Locate and identify every blood parasite.
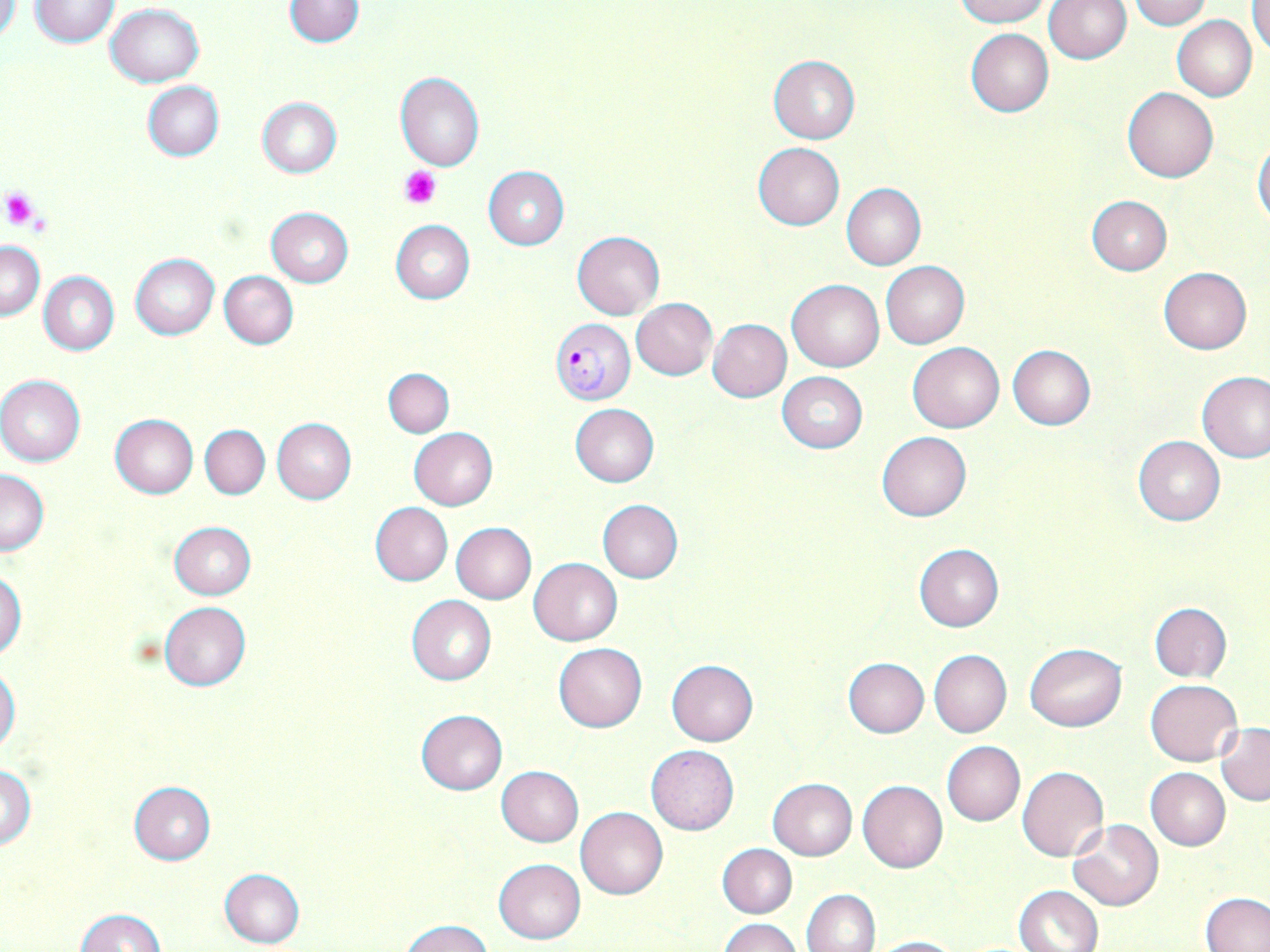
Approximate bounding boxes as (x1,y1)-(x2,y2) corner pairs in pixels.
Plasmodium falciparum-infected red blood cells: (549,318)-(634,404).
No Plasmodium ovale, Plasmodium malariae, Plasmodium vivax, Babesia divergens, or Trypanosoma brucei observed.

slide-level diagnosis = Plasmodium falciparum
preparation = thin blood smear
image size = 1270×952 pixels
stain = May-Grünwald-Giemsa
field of view = single
modality = optical microscopy
magnification = 1000x
uninfected red blood cell locations = approximate bounding boxes as (x1,y1)-(x2,y2) corner pairs in pixels: (0,0)-(21,45), (28,0)-(121,47), (283,0)-(365,48), (954,0)-(1049,26), (1045,0)-(1131,63), (1128,0)-(1212,30), (1250,3)-(1270,56), (106,4)-(205,86), (1172,16)-(1257,101), (964,28)-(1054,117), (769,55)-(859,144), (394,71)-(484,171), (142,81)-(224,161), (1123,87)-(1218,182), (256,98)-(341,178), (1253,138)-(1270,229), (753,142)-(845,229), (483,166)-(569,249), (842,183)-(926,269), (1087,195)-(1172,275), (265,207)-(354,287), (392,220)-(474,303), (571,231)-(665,319), (1,239)-(44,320), (130,253)-(220,340), (881,261)-(969,348), (1158,268)-(1251,354), (39,271)-(119,356), (219,271)-(299,349), (787,278)-(884,371), (631,298)-(717,380), (709,319)-(792,402), (908,341)-(1004,433), (1007,344)-(1096,430), (382,367)-(454,437), (776,372)-(867,453), (1197,372)-(1270,463), (0,374)-(85,467), (570,403)-(659,486), (109,414)-(198,499), (272,419)-(356,504), (201,425)-(269,499), (409,428)-(497,509), (877,431)-(971,521), (1133,434)-(1225,526), (0,469)-(50,555), (597,499)-(683,584), (370,502)-(452,586), (167,521)-(255,600), (451,523)-(537,603), (913,544)-(1003,632), (529,558)-(622,645), (0,570)-(26,658), (406,594)-(497,686), (159,601)-(252,691), (1149,602)-(1231,682), (553,643)-(647,732), (1024,643)-(1126,731), (930,650)-(1012,738), (843,657)-(929,737), (667,659)-(758,745), (0,665)-(21,755), (1146,679)-(1242,766), (415,710)-(508,795), (1217,723)-(1270,805), (941,741)-(1024,826), (646,745)-(740,835), (0,764)-(36,849), (497,766)-(583,846), (1017,766)-(1109,861), (1146,767)-(1230,850), (768,778)-(858,860), (858,780)-(947,873), (128,781)-(216,864), (577,807)-(668,898), (1068,819)-(1163,910), (717,843)-(797,918), (494,858)-(585,943), (218,868)-(305,948), (1014,886)-(1103,952), (803,889)-(881,952), (1202,893)-(1269,952), (76,909)-(166,951), (720,918)-(803,952), (403,919)-(492,952), (867,935)-(961,952)
platelet locations = approximate bounding boxes as (x1,y1)-(x2,y2) corner pairs in pixels: (400,166)-(441,207), (0,188)-(39,231)